Give the extent of all Trypanosoma brucei.
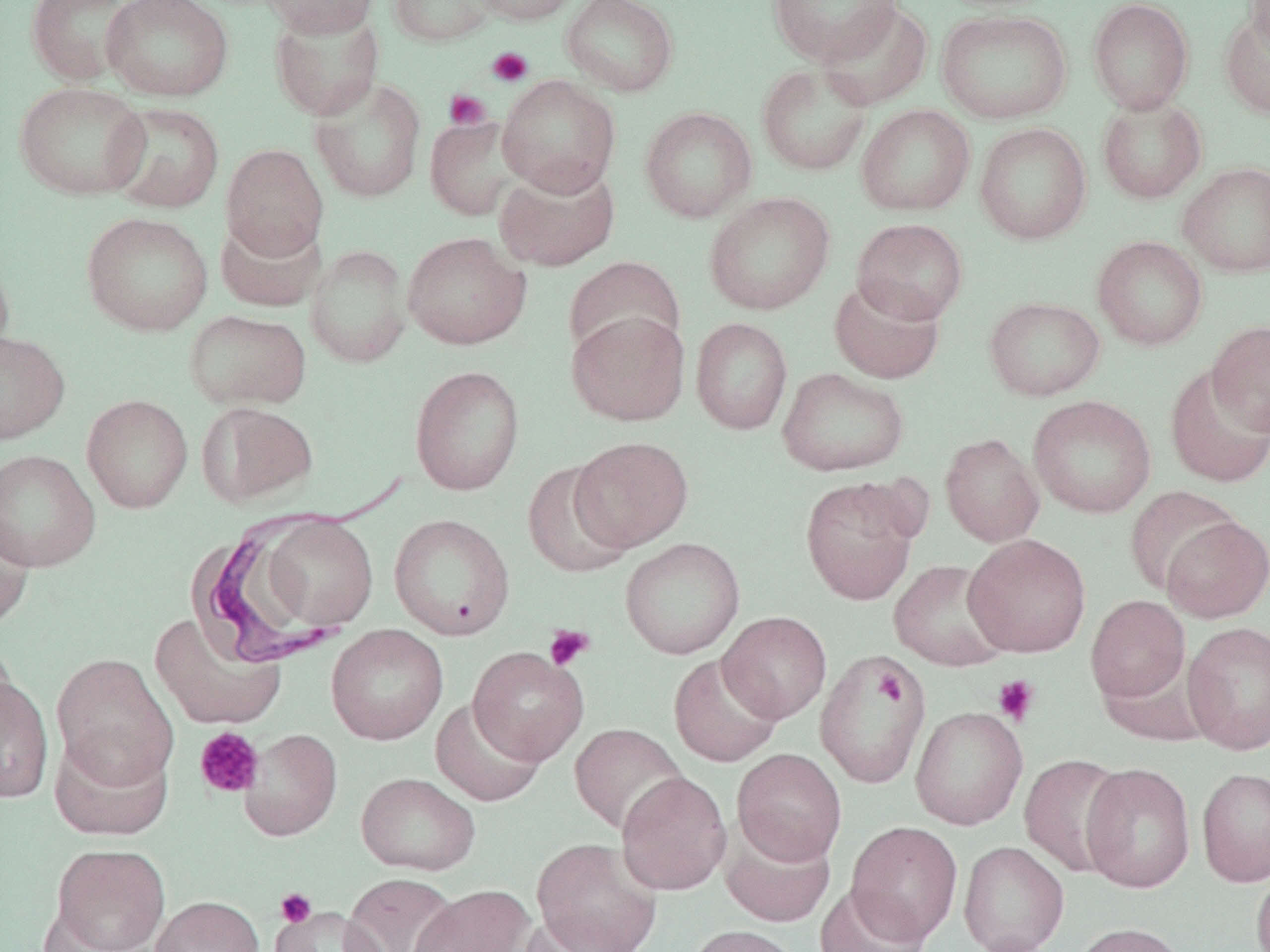
Approximate bounding boxes as named x1/y1/x2/y2 corners in pixels.
Trypanosoma brucei: (x1=194, y1=461, x2=413, y2=664).

Uninfected red blood cell locations: (x1=26, y1=0, x2=136, y2=86), (x1=102, y1=0, x2=233, y2=102), (x1=261, y1=0, x2=380, y2=37), (x1=387, y1=0, x2=501, y2=47), (x1=472, y1=0, x2=582, y2=25), (x1=561, y1=0, x2=679, y2=98), (x1=767, y1=0, x2=903, y2=65), (x1=1087, y1=0, x2=1193, y2=114), (x1=1245, y1=0, x2=1270, y2=60), (x1=816, y1=1, x2=933, y2=111), (x1=269, y1=7, x2=385, y2=121), (x1=1218, y1=7, x2=1270, y2=120), (x1=936, y1=9, x2=1073, y2=124), (x1=756, y1=62, x2=873, y2=176), (x1=497, y1=75, x2=621, y2=196), (x1=309, y1=76, x2=427, y2=204), (x1=14, y1=81, x2=151, y2=201), (x1=1096, y1=95, x2=1207, y2=204), (x1=106, y1=102, x2=225, y2=213), (x1=855, y1=104, x2=975, y2=216), (x1=639, y1=107, x2=757, y2=223), (x1=425, y1=115, x2=526, y2=220), (x1=974, y1=122, x2=1092, y2=245), (x1=221, y1=144, x2=328, y2=261), (x1=1178, y1=161, x2=1270, y2=278), (x1=495, y1=163, x2=620, y2=271), (x1=703, y1=192, x2=835, y2=315), (x1=81, y1=211, x2=214, y2=336), (x1=216, y1=215, x2=325, y2=312), (x1=851, y1=218, x2=969, y2=324), (x1=401, y1=232, x2=531, y2=349), (x1=1092, y1=236, x2=1208, y2=350), (x1=306, y1=243, x2=412, y2=369), (x1=0, y1=251, x2=15, y2=370), (x1=564, y1=256, x2=685, y2=362), (x1=829, y1=276, x2=945, y2=384), (x1=983, y1=296, x2=1105, y2=401), (x1=184, y1=309, x2=311, y2=410), (x1=567, y1=310, x2=690, y2=426), (x1=691, y1=317, x2=793, y2=435), (x1=1207, y1=320, x2=1270, y2=435), (x1=0, y1=329, x2=69, y2=444), (x1=1164, y1=363, x2=1270, y2=488), (x1=409, y1=364, x2=525, y2=495), (x1=777, y1=367, x2=909, y2=477), (x1=82, y1=394, x2=193, y2=513), (x1=1028, y1=395, x2=1156, y2=518), (x1=196, y1=401, x2=318, y2=508), (x1=940, y1=433, x2=1044, y2=547), (x1=569, y1=436, x2=693, y2=551), (x1=0, y1=449, x2=100, y2=572), (x1=522, y1=462, x2=635, y2=578), (x1=799, y1=477, x2=919, y2=605), (x1=1125, y1=486, x2=1242, y2=596), (x1=0, y1=507, x2=35, y2=631), (x1=388, y1=513, x2=515, y2=640), (x1=260, y1=515, x2=379, y2=631), (x1=1160, y1=515, x2=1269, y2=623), (x1=964, y1=534, x2=1091, y2=657), (x1=620, y1=537, x2=745, y2=659), (x1=889, y1=560, x2=1012, y2=671), (x1=1085, y1=595, x2=1191, y2=703), (x1=718, y1=611, x2=832, y2=723), (x1=149, y1=612, x2=287, y2=730), (x1=1183, y1=621, x2=1270, y2=755), (x1=326, y1=624, x2=448, y2=745), (x1=0, y1=635, x2=18, y2=736), (x1=467, y1=647, x2=588, y2=765), (x1=815, y1=651, x2=930, y2=788), (x1=51, y1=653, x2=178, y2=788), (x1=668, y1=653, x2=785, y2=768), (x1=0, y1=674, x2=54, y2=803), (x1=431, y1=697, x2=546, y2=807), (x1=910, y1=706, x2=1028, y2=830), (x1=569, y1=723, x2=688, y2=836), (x1=239, y1=729, x2=342, y2=841), (x1=49, y1=730, x2=174, y2=841), (x1=732, y1=748, x2=847, y2=865), (x1=1019, y1=753, x2=1130, y2=877), (x1=1080, y1=763, x2=1196, y2=893), (x1=1196, y1=767, x2=1270, y2=888), (x1=616, y1=771, x2=732, y2=895), (x1=356, y1=772, x2=480, y2=875), (x1=720, y1=821, x2=836, y2=927), (x1=845, y1=821, x2=963, y2=946), (x1=530, y1=836, x2=663, y2=952), (x1=958, y1=841, x2=1069, y2=952), (x1=50, y1=843, x2=170, y2=952), (x1=1251, y1=865, x2=1270, y2=952), (x1=341, y1=873, x2=460, y2=952), (x1=814, y1=884, x2=930, y2=952), (x1=408, y1=885, x2=534, y2=952), (x1=150, y1=895, x2=264, y2=952), (x1=270, y1=906, x2=386, y2=952), (x1=515, y1=914, x2=638, y2=952), (x1=1070, y1=922, x2=1190, y2=952), (x1=685, y1=924, x2=803, y2=952). Platelet locations: (x1=486, y1=47, x2=533, y2=86), (x1=444, y1=89, x2=491, y2=130), (x1=147, y1=613, x2=283, y2=731), (x1=544, y1=625, x2=594, y2=671), (x1=874, y1=670, x2=907, y2=706), (x1=992, y1=675, x2=1041, y2=725), (x1=195, y1=727, x2=264, y2=798), (x1=275, y1=888, x2=316, y2=927). Slide-level diagnosis: Trypanosoma brucei. Thin blood smear. May-Grünwald-Giemsa stain. Optical microscopy. Image is 1270×952 pixels. 1000x magnification. One field of a larger specimen.